Name the blood parasite species.
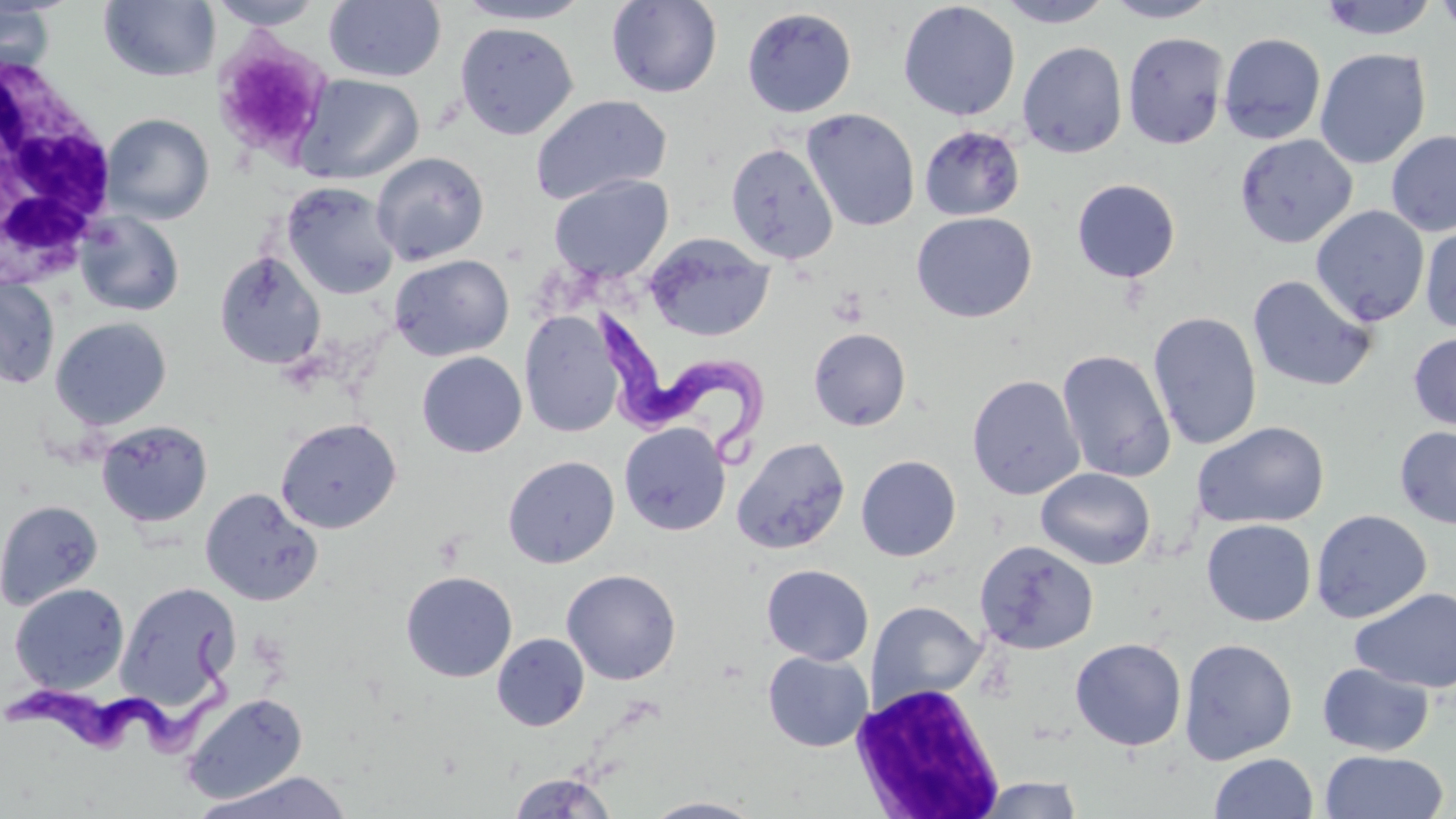
Trypanosoma brucei.

Summary:
  - Coordinate format: approximate bounding boxes as (x1,y1)-(x2,y2) corner pairs in pixels
  - Uninfected red blood cell locations: (99,0)-(220,82), (206,0)-(327,31), (323,0)-(446,83), (452,0)-(596,25), (606,0)-(723,98), (995,0)-(1116,28), (1103,0)-(1221,23), (1316,0)-(1440,41), (1433,0)-(1456,39), (897,1)-(1020,121), (0,2)-(57,79), (742,7)-(857,117), (455,21)-(579,140), (1123,32)-(1229,150), (1218,33)-(1326,145), (211,35)-(335,163), (1017,42)-(1128,158), (1314,48)-(1431,170), (293,74)-(424,185), (530,94)-(672,206), (802,109)-(920,232), (101,113)-(215,224), (918,124)-(1025,221), (1386,129)-(1456,237), (1234,134)-(1357,249), (726,142)-(838,264), (371,151)-(489,266), (548,174)-(674,282), (1072,179)-(1181,283), (280,181)-(401,299), (1311,205)-(1430,327), (76,211)-(185,317), (911,212)-(1037,323), (1420,221)-(1456,335), (645,233)-(775,342), (213,250)-(327,371), (389,253)-(514,361), (1247,274)-(1378,393), (0,276)-(61,389), (519,310)-(623,438), (1148,311)-(1263,451), (50,316)-(173,431), (808,327)-(912,431), (1408,331)-(1456,432), (1056,349)-(1175,483), (416,351)-(527,457), (967,374)-(1085,500), (275,418)-(402,534), (96,419)-(214,528), (1193,421)-(1330,529), (619,422)-(731,536), (1394,426)-(1456,529), (731,436)-(850,555), (502,455)-(620,568), (855,455)-(962,561), (1036,468)-(1156,570), (200,487)-(324,606), (0,498)-(104,610), (1310,509)-(1432,624), (1202,518)-(1317,626), (973,540)-(1098,654), (761,564)-(874,666), (561,569)-(682,685), (400,570)-(518,682), (115,580)-(241,712), (9,582)-(130,694), (1350,587)-(1456,693), (866,601)-(986,709), (492,633)-(589,731), (1070,637)-(1187,751), (1180,639)-(1297,764), (762,651)-(873,752), (1317,662)-(1435,756), (181,692)-(308,804), (1320,749)-(1448,818), (1209,752)-(1318,818), (192,770)-(355,819), (508,772)-(617,818), (974,776)-(1085,818), (641,796)-(766,818)
  - Platelet locations: (828,287)-(869,328)
  - Trypanosoma brucei locations: (599,297)-(770,463), (0,623)-(232,762)
  - White blood cell locations: (0,47)-(117,290), (851,682)-(1007,818)
  - Image size: 1456×819 pixels
  - Field of view: one of a larger specimen
  - Modality: optical microscopy
  - Preparation: thin blood film
  - Stain: May-Grünwald-Giemsa
  - Magnification: 1000x